Classify this cell by malaria status.
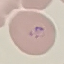
It is parasitized.

Thin smear of blood. Giemsa-stained preparation. Photographed with a smartphone camera at the microscope eyepiece. Cell patch, automatically extracted from a larger field of view and resized to 64 × 64 pixels.